State which parasite is depicted.
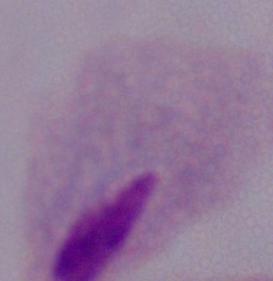
This is a trichomonad.

Micrograph. 1000x magnification.